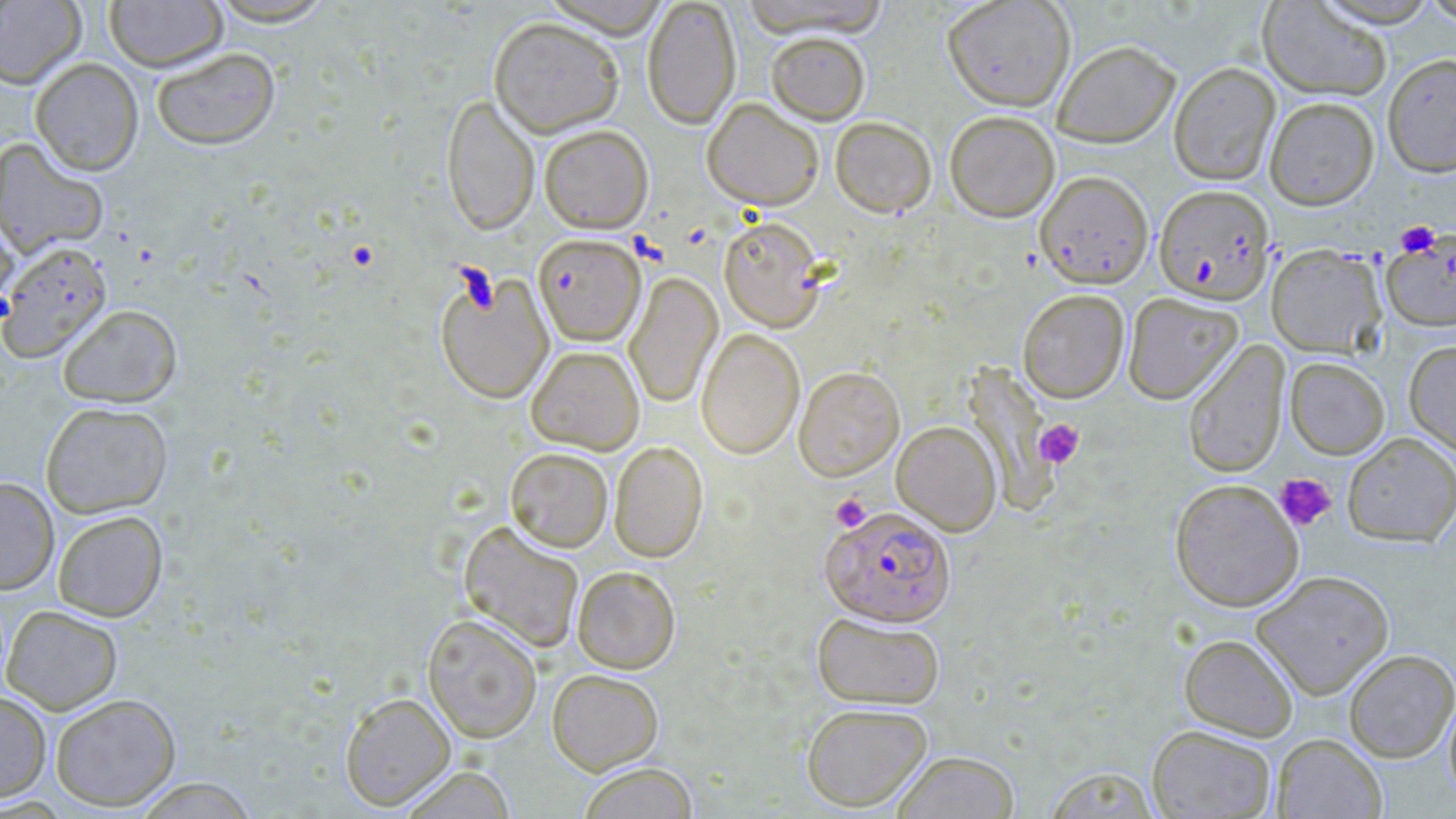

Summary:
  - Coordinate format: approximate bounding boxes as [x1, y1, x2, y2] in pixels
  - Platelet locations: [1394, 221, 1441, 257], [1034, 419, 1084, 468], [1274, 473, 1337, 531], [830, 493, 871, 532]
  - Plasmodium falciparum-infected red blood cell locations: [1153, 184, 1275, 304], [533, 233, 646, 346], [820, 505, 956, 626]
  - Uninfected red blood cell locations: [0, 0, 86, 88], [203, 0, 339, 27], [541, 0, 671, 38], [642, 0, 741, 129], [737, 0, 892, 38], [942, 0, 1076, 111], [1312, 0, 1443, 27], [1419, 0, 1456, 26], [104, 1, 228, 72], [1257, 1, 1392, 101], [488, 16, 625, 137], [766, 32, 871, 124], [1052, 40, 1180, 146], [150, 46, 280, 150], [1382, 53, 1456, 177], [29, 58, 144, 176], [1168, 62, 1281, 186], [441, 93, 540, 235], [1264, 96, 1379, 210], [702, 98, 824, 210], [945, 111, 1060, 222], [830, 116, 936, 217], [539, 124, 653, 233], [0, 138, 109, 258], [1035, 170, 1154, 289], [0, 211, 19, 322], [718, 215, 826, 332], [1382, 233, 1456, 332], [0, 241, 112, 362], [1265, 243, 1386, 359], [435, 271, 554, 404], [624, 272, 722, 409], [1017, 289, 1129, 402], [1122, 293, 1242, 404], [57, 304, 182, 407], [695, 328, 805, 460], [1404, 340, 1456, 457], [1183, 341, 1290, 478], [526, 345, 645, 455], [1285, 357, 1390, 459], [793, 366, 904, 481], [40, 401, 172, 518], [892, 421, 1001, 536], [1342, 433, 1456, 546], [609, 441, 708, 562], [505, 447, 613, 552], [0, 476, 59, 595], [1169, 478, 1304, 611], [52, 510, 168, 621], [458, 521, 584, 653], [572, 565, 681, 673], [1251, 570, 1395, 699], [1, 605, 123, 715], [811, 612, 944, 709], [422, 613, 542, 743], [1179, 633, 1299, 741], [1343, 649, 1456, 763], [547, 668, 664, 774], [1444, 688, 1456, 807], [0, 690, 52, 802], [340, 692, 456, 811], [50, 693, 181, 811], [800, 702, 933, 812], [1147, 724, 1277, 818], [1272, 733, 1386, 818], [891, 750, 1020, 818], [577, 762, 699, 818], [398, 765, 517, 818], [1043, 765, 1161, 818], [132, 778, 260, 818]
  - Slide-level diagnosis: Plasmodium falciparum
  - Field of view: one of a larger specimen
  - Stain: May-Grünwald-Giemsa
  - Modality: light microscopy
  - Magnification: 1000x
  - Preparation: thin blood smear
  - Image size: 1456×819 pixels